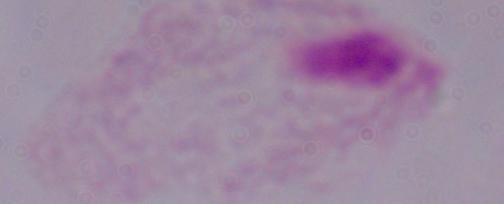

Summary:
  - Modality: micrograph
  - Magnification: 1000x
  - Identification: trichomonad